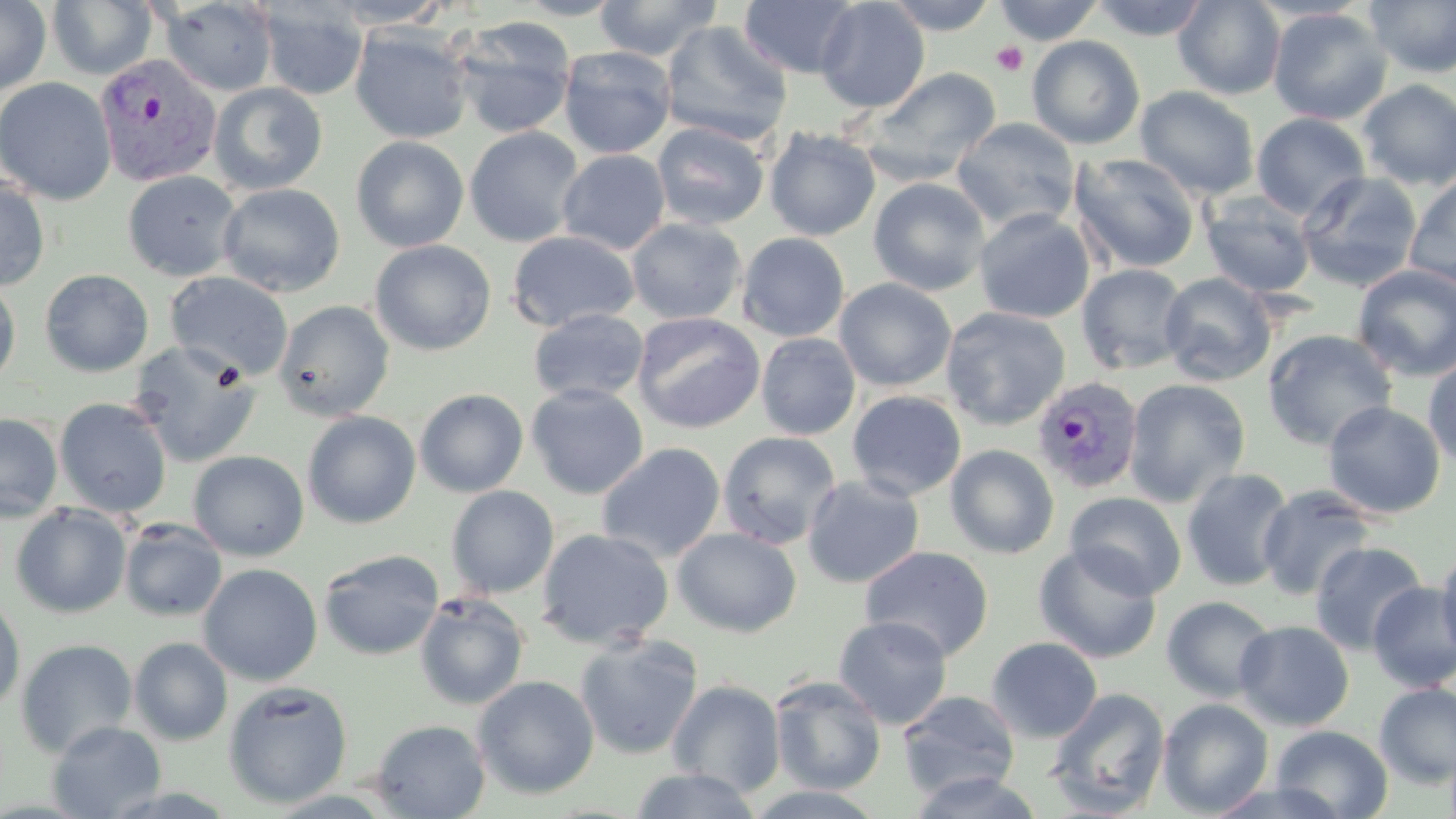

Summary:
  - Coordinate format: approximate bounding boxes as (x1,y1)-(x2,y2) corner pairs in pixels
  - Uninfected red blood cell locations: (0,0)-(51,96), (45,0)-(159,81), (512,0)-(628,20), (594,0)-(722,61), (739,0)-(861,79), (815,0)-(930,113), (882,0)-(1000,34), (993,0)-(1105,45), (1090,0)-(1211,41), (1173,0)-(1286,100), (159,1)-(278,97), (321,1)-(454,29), (1365,1)-(1456,78), (257,2)-(369,101), (1268,7)-(1392,125), (451,17)-(577,139), (659,20)-(794,146), (349,25)-(474,144), (1027,35)-(1146,150), (558,45)-(677,159), (860,67)-(1002,185), (0,77)-(117,204), (1358,80)-(1456,190), (208,82)-(328,196), (1135,86)-(1260,200), (1251,112)-(1371,220), (951,117)-(1080,234), (652,121)-(770,230), (464,126)-(584,247), (765,127)-(881,241), (351,136)-(469,253), (557,149)-(671,255), (1069,152)-(1201,275), (122,170)-(242,282), (1296,170)-(1423,292), (1403,173)-(1456,291), (0,175)-(51,292), (868,177)-(991,296), (217,183)-(346,298), (1200,193)-(1317,298), (974,208)-(1095,323), (626,218)-(747,325), (506,230)-(639,333), (737,232)-(850,342), (369,240)-(496,356), (1077,263)-(1190,375), (1352,264)-(1456,382), (39,269)-(153,377), (165,271)-(294,381), (1159,272)-(1277,386), (834,278)-(956,391), (0,279)-(21,387), (274,299)-(395,421), (940,307)-(1071,430), (528,308)-(649,405), (632,312)-(765,434), (1261,329)-(1398,451), (756,333)-(861,440), (127,339)-(262,467), (1422,354)-(1456,473), (1123,378)-(1251,507), (526,383)-(649,500), (414,388)-(529,497), (847,390)-(966,501), (54,398)-(172,518), (1323,401)-(1446,519), (302,410)-(421,529), (0,413)-(63,522), (718,431)-(842,550), (596,443)-(726,563), (945,444)-(1060,559), (188,450)-(310,561), (1181,467)-(1296,591), (801,474)-(925,589), (1256,484)-(1378,601), (446,486)-(559,598), (1065,492)-(1187,600), (10,504)-(132,618), (119,519)-(227,622), (672,527)-(802,637), (535,528)-(674,649), (1310,541)-(1428,655), (1033,543)-(1163,664), (1436,543)-(1456,666), (860,545)-(994,661), (318,548)-(444,661), (197,563)-(323,686), (1367,582)-(1456,692), (414,592)-(529,710), (0,595)-(26,713), (1161,595)-(1276,703), (833,615)-(953,729), (1233,620)-(1354,731), (574,634)-(703,760), (129,637)-(233,745), (986,637)-(1103,744), (15,638)-(138,758), (472,675)-(599,799), (769,676)-(886,795), (666,679)-(786,798), (223,680)-(353,808), (1374,682)-(1456,789), (1046,687)-(1171,817), (897,691)-(1020,801), (1157,698)-(1273,817), (369,719)-(490,818), (47,720)-(166,819), (1270,725)-(1394,818), (627,768)-(763,818), (907,770)-(1044,818), (1205,780)-(1348,818)
  - Plasmodium vivax-infected red blood cell locations: (94,53)-(223,187), (1031,376)-(1143,495)
  - Platelet locations: (991,41)-(1029,76)
  - Slide-level diagnosis: Plasmodium vivax
  - Stain: May-Grünwald-Giemsa
  - Preparation: thin blood film
  - Field of view: single
  - Image size: 1456×819 pixels
  - Modality: optical microscopy
  - Magnification: 1000x